State the preparation type.
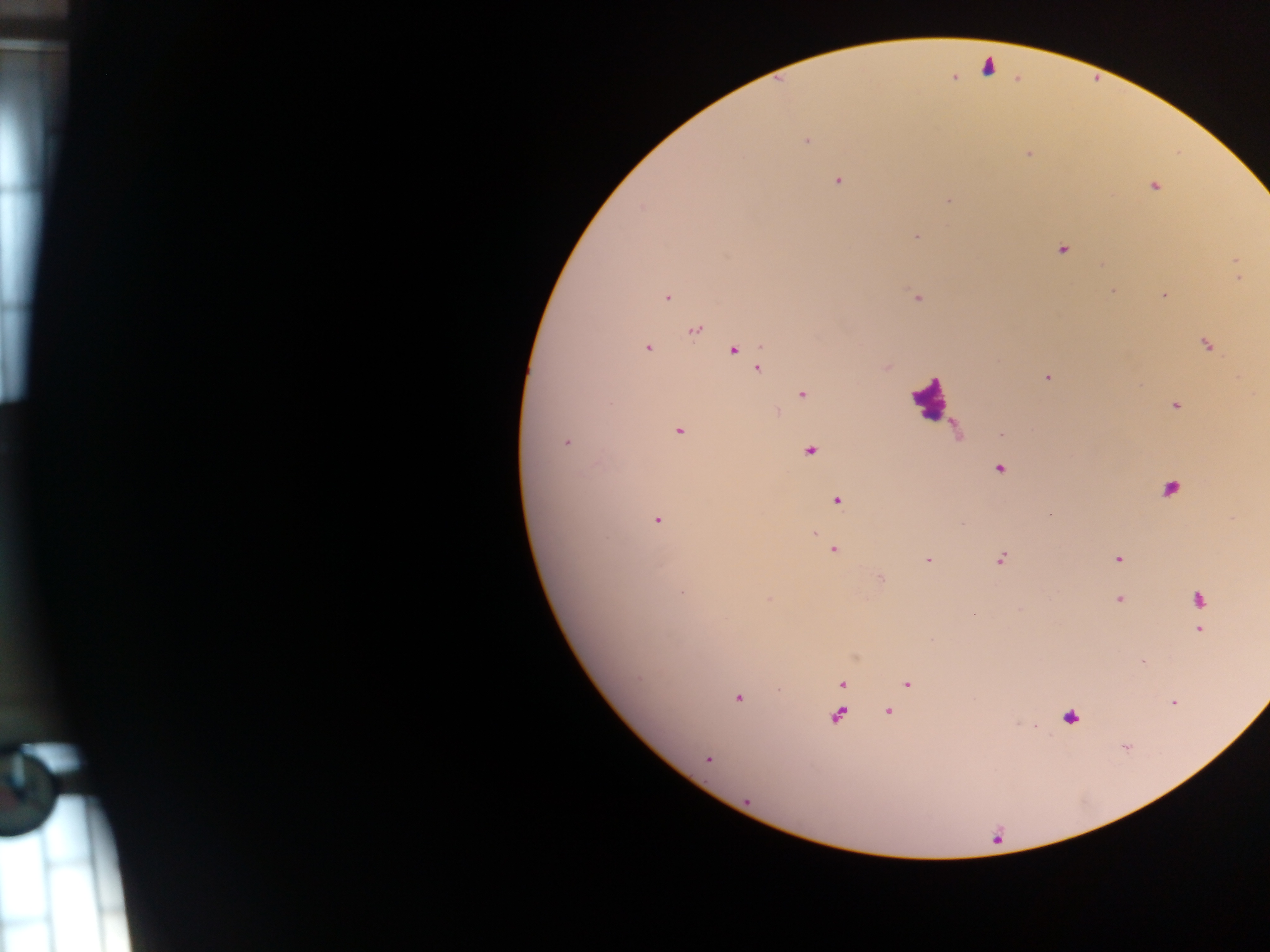

Thick blood film.

Approximate centers as (x, y) in pixels.
Summary:
  - Plasmodium parasite locations: (987, 67), (954, 78), (807, 141), (1027, 154), (838, 181), (1155, 186), (948, 201), (916, 236), (1062, 250), (1236, 262), (1239, 278), (1113, 292), (1163, 295), (667, 298), (917, 298), (694, 330), (1206, 345), (648, 348), (733, 350), (887, 367), (757, 368), (1047, 378), (803, 394), (1174, 405), (679, 431), (566, 443), (811, 451), (998, 470), (1170, 489), (836, 500), (1049, 515), (657, 520), (814, 533), (833, 550), (1117, 558), (1001, 559), (928, 560), (881, 578), (682, 593), (1199, 599), (1119, 600), (1201, 630), (1142, 661), (908, 683), (842, 684), (738, 698), (1173, 702), (888, 712), (838, 715), (1069, 718), (1125, 747), (708, 759)
  - Leukocyte locations: (930, 397)
  - Capture: mobile-phone photograph through a microscope
  - Field of view: single
  - Country: Ghana
  - Image size: 1270×952 pixels